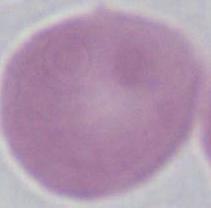
An erythrocyte is shown. Captured at 1000x magnification. Micrograph.